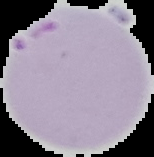
Summary:
  - Image size: 154×157 pixels
  - Result: Plasmodium parasites identified
  - Image type: cell region segmented out of the field of view; surrounding area masked to black
  - Preparation: thin blood film